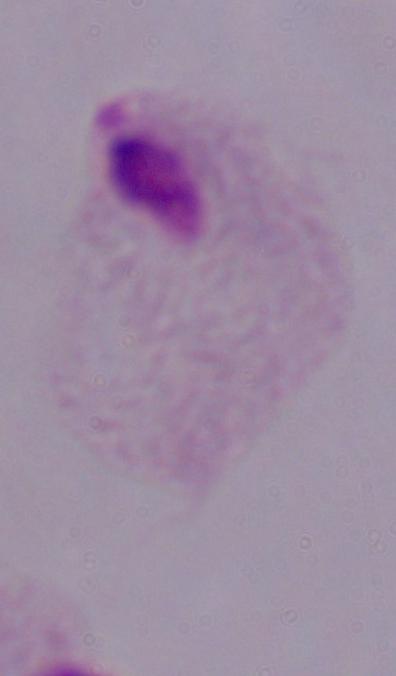
{
  "modality": "micrograph",
  "identification": "trichomonad",
  "magnification": "1000x"
}